Locate every malaria parasite.
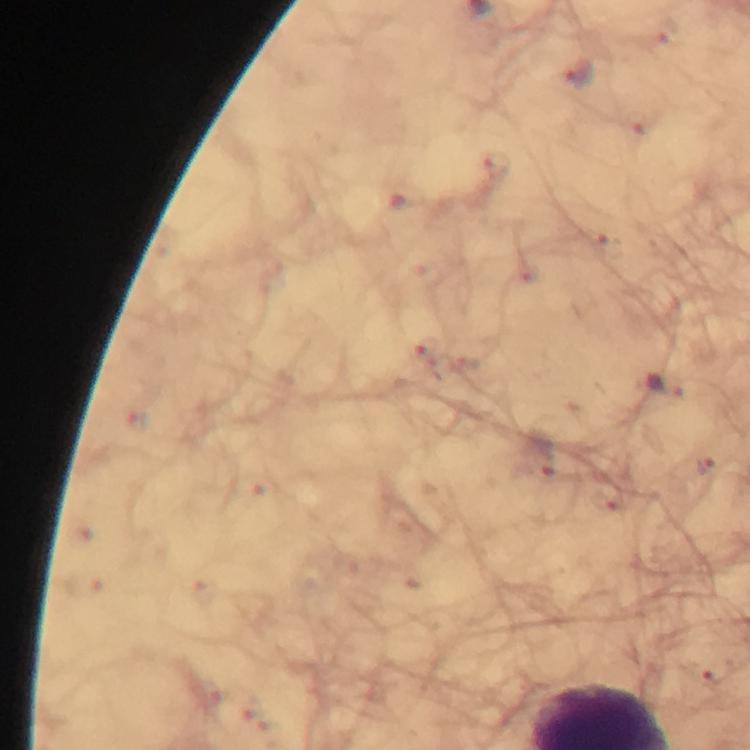
Approximate object centers, in pixels from the top-left corner.
Malaria parasites: (x=579, y=76), (x=667, y=383), (x=542, y=456), (x=704, y=466).

{
  "cropped_from": "one field of view",
  "magnification": "100x",
  "context": "from a malaria diagnostic workup",
  "stain": "Giemsa",
  "image_size": "750×750 pixels",
  "immersion_oil": "used",
  "preparation": "thick blood film",
  "capture": "smartphone mounted on the microscope"
}